Report the malaria status of this cell.
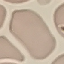

Uninfected.

Acquired by smartphone through the microscope eyepiece. Automatically extracted cell patch, resized to 64 × 64 pixels. Thin blood film. Giemsa-stained preparation.